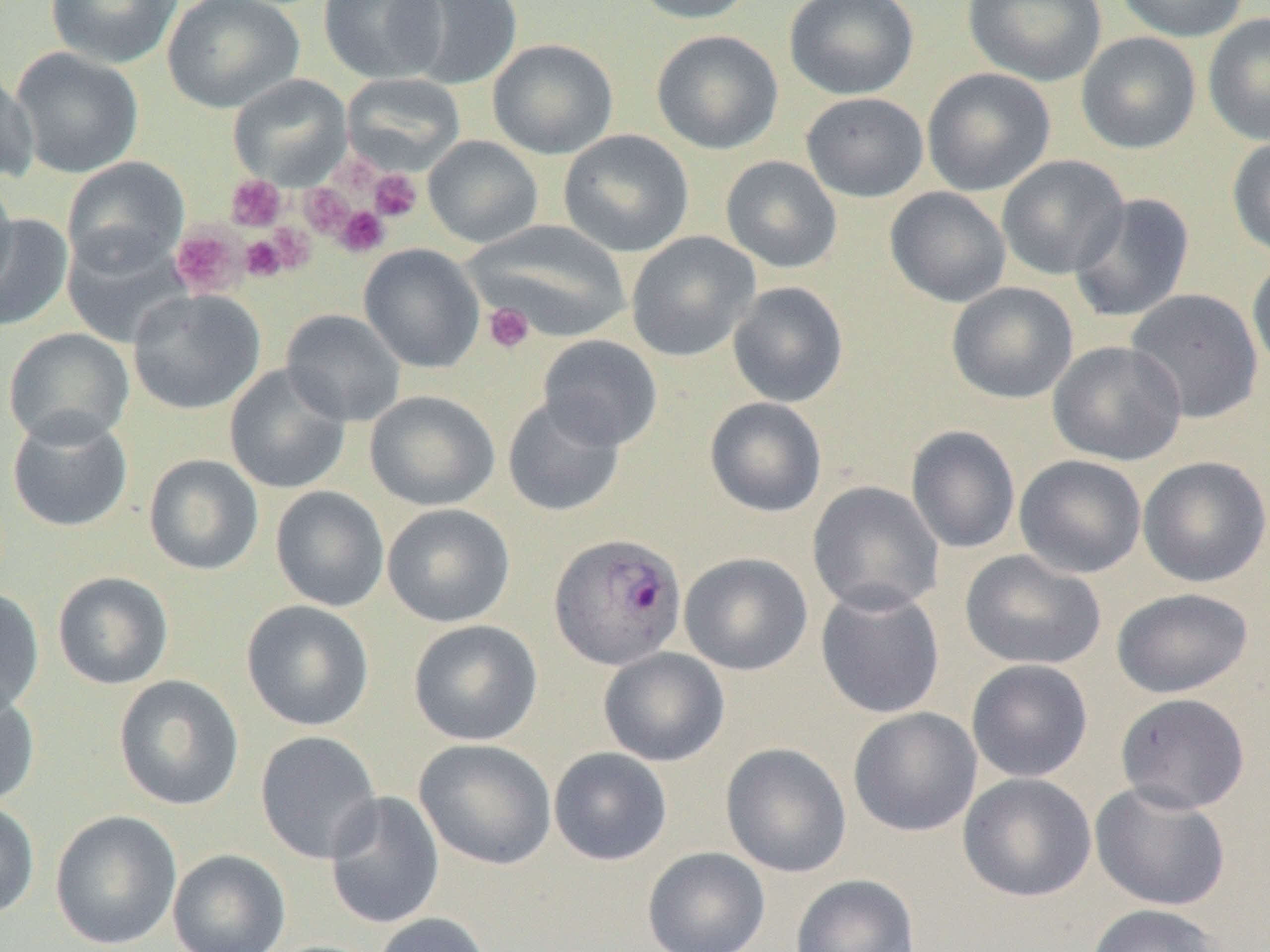
Approximate bounding boxes as [x1, y1, x2, y2] in pixels. Plasmodium ovale-infected red blood cell locations: [549, 533, 687, 670]. Platelet locations: [331, 158, 378, 194], [369, 169, 422, 222], [225, 175, 285, 231], [300, 185, 355, 236], [334, 205, 390, 257], [266, 221, 317, 275], [170, 225, 246, 298], [240, 235, 287, 282], [483, 303, 534, 354]. Uninfected red blood cell locations: [45, 0, 183, 69], [162, 0, 304, 113], [319, 0, 446, 83], [394, 0, 523, 90], [627, 0, 760, 24], [784, 0, 919, 100], [963, 0, 1107, 87], [1114, 0, 1249, 42], [1203, 13, 1270, 146], [651, 30, 783, 154], [1076, 32, 1202, 154], [487, 38, 619, 159], [10, 47, 144, 178], [0, 66, 38, 183], [921, 67, 1056, 196], [228, 74, 352, 189], [342, 74, 465, 171], [801, 92, 929, 202], [558, 130, 694, 257], [423, 136, 543, 248], [1226, 136, 1270, 258], [720, 155, 842, 274], [996, 155, 1129, 280], [62, 156, 190, 275], [0, 171, 17, 301], [885, 187, 1011, 307], [1069, 193, 1195, 323], [0, 214, 73, 331], [466, 220, 632, 343], [62, 230, 190, 348], [626, 231, 761, 362], [359, 244, 485, 373], [1247, 253, 1270, 377], [727, 281, 849, 407], [946, 282, 1078, 404], [1125, 288, 1264, 424], [127, 289, 265, 414], [281, 309, 406, 426], [3, 327, 134, 447], [537, 335, 663, 451], [1047, 340, 1187, 466], [224, 364, 351, 494], [365, 390, 500, 510], [502, 396, 626, 517], [704, 397, 827, 517], [7, 410, 133, 533], [906, 425, 1021, 554], [143, 454, 264, 576], [1014, 454, 1146, 579], [1138, 455, 1270, 587], [806, 481, 944, 616], [270, 486, 390, 612], [382, 503, 515, 628], [959, 550, 1107, 671], [679, 552, 813, 676], [52, 571, 174, 690], [815, 584, 946, 719], [1111, 587, 1253, 698], [0, 588, 45, 717], [241, 600, 375, 731], [408, 619, 543, 745], [599, 647, 730, 767], [966, 659, 1093, 782], [113, 674, 244, 811], [0, 684, 40, 808], [1114, 692, 1250, 814], [848, 707, 982, 837], [255, 730, 382, 864], [414, 738, 557, 870], [721, 742, 852, 878], [548, 747, 672, 865], [957, 772, 1097, 902], [1090, 782, 1231, 912], [324, 790, 445, 930], [0, 799, 40, 920], [49, 810, 182, 950], [642, 847, 770, 952], [167, 849, 291, 952], [790, 874, 920, 952], [1086, 904, 1226, 952], [371, 912, 495, 952]. Slide-level diagnosis: Plasmodium ovale. Thin blood film. Captured at 1000x magnification. Image is 1270×952 pixels. Light microscopy. One field of a larger specimen.